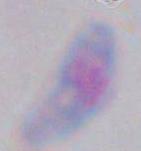

Summary:
  - Modality: photomicrograph
  - Identification: Toxoplasma gondii
  - Magnification: 1000x